Report the malaria status of this cell.
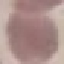
Uninfected.

Photographed with a smartphone camera at the microscope eyepiece. Giemsa-stained preparation. Thin smear of blood. Cell patch, automatically extracted from a larger field of view and resized to 64 × 64 pixels.